Identify the blood parasite species.
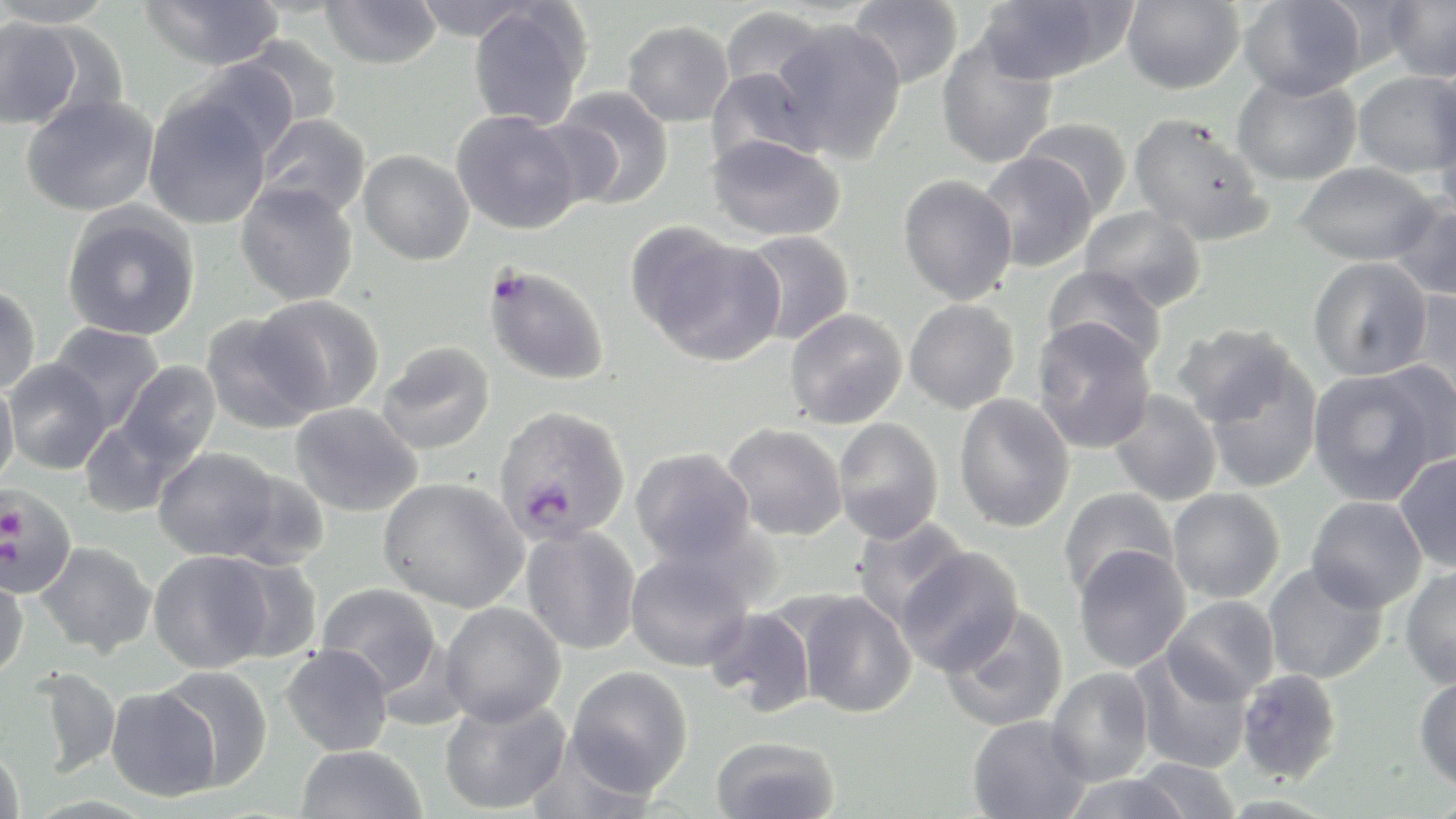

Plasmodium falciparum.

Approximate bounding boxes as named x1/y1/x2/y2 corners in pixels. Uninfected red blood cell locations: (x1=0, y1=0, x2=119, y2=28), (x1=139, y1=0, x2=285, y2=70), (x1=321, y1=0, x2=442, y2=69), (x1=409, y1=0, x2=537, y2=42), (x1=847, y1=0, x2=964, y2=91), (x1=976, y1=0, x2=1130, y2=84), (x1=1121, y1=0, x2=1244, y2=94), (x1=1316, y1=0, x2=1421, y2=74), (x1=1383, y1=0, x2=1456, y2=83), (x1=1238, y1=1, x2=1368, y2=100), (x1=467, y1=3, x2=592, y2=131), (x1=718, y1=5, x2=833, y2=104), (x1=0, y1=17, x2=83, y2=130), (x1=622, y1=20, x2=733, y2=127), (x1=770, y1=20, x2=907, y2=163), (x1=233, y1=33, x2=345, y2=131), (x1=936, y1=36, x2=1059, y2=169), (x1=181, y1=60, x2=299, y2=162), (x1=705, y1=66, x2=822, y2=169), (x1=1352, y1=71, x2=1455, y2=178), (x1=1231, y1=73, x2=1362, y2=186), (x1=551, y1=86, x2=675, y2=210), (x1=143, y1=91, x2=273, y2=230), (x1=20, y1=94, x2=159, y2=217), (x1=1431, y1=96, x2=1456, y2=222), (x1=451, y1=110, x2=583, y2=235), (x1=1129, y1=112, x2=1271, y2=245), (x1=255, y1=114, x2=371, y2=220), (x1=1019, y1=117, x2=1132, y2=219), (x1=705, y1=133, x2=846, y2=241), (x1=358, y1=149, x2=474, y2=265), (x1=977, y1=151, x2=1098, y2=272), (x1=1294, y1=161, x2=1438, y2=266), (x1=898, y1=174, x2=1018, y2=305), (x1=235, y1=181, x2=359, y2=306), (x1=1388, y1=196, x2=1456, y2=302), (x1=61, y1=204, x2=201, y2=341), (x1=1079, y1=204, x2=1207, y2=311), (x1=629, y1=225, x2=784, y2=367), (x1=740, y1=230, x2=855, y2=345), (x1=1308, y1=257, x2=1433, y2=382), (x1=1042, y1=264, x2=1168, y2=369), (x1=0, y1=284, x2=41, y2=395), (x1=1399, y1=289, x2=1456, y2=410), (x1=252, y1=294, x2=385, y2=417), (x1=904, y1=299, x2=1020, y2=413), (x1=784, y1=308, x2=909, y2=429), (x1=199, y1=310, x2=323, y2=433), (x1=1031, y1=319, x2=1157, y2=453), (x1=48, y1=323, x2=165, y2=431), (x1=1172, y1=323, x2=1301, y2=429), (x1=376, y1=341, x2=496, y2=455), (x1=1199, y1=351, x2=1323, y2=493), (x1=1369, y1=358, x2=1456, y2=471), (x1=2, y1=359, x2=111, y2=474), (x1=118, y1=361, x2=221, y2=466), (x1=1308, y1=369, x2=1444, y2=506), (x1=0, y1=378, x2=19, y2=487), (x1=1109, y1=389, x2=1223, y2=507), (x1=953, y1=393, x2=1075, y2=533), (x1=289, y1=401, x2=424, y2=517), (x1=78, y1=417, x2=187, y2=518), (x1=833, y1=417, x2=944, y2=544), (x1=721, y1=422, x2=847, y2=541), (x1=153, y1=446, x2=280, y2=561), (x1=630, y1=447, x2=756, y2=567), (x1=1394, y1=453, x2=1456, y2=573), (x1=222, y1=468, x2=331, y2=571), (x1=378, y1=477, x2=529, y2=612), (x1=1058, y1=487, x2=1178, y2=598), (x1=1167, y1=488, x2=1285, y2=603), (x1=1305, y1=495, x2=1428, y2=613), (x1=850, y1=516, x2=970, y2=630), (x1=521, y1=526, x2=641, y2=654), (x1=35, y1=541, x2=157, y2=657), (x1=1073, y1=545, x2=1191, y2=672), (x1=895, y1=546, x2=1025, y2=676), (x1=625, y1=549, x2=755, y2=672), (x1=148, y1=550, x2=274, y2=673), (x1=216, y1=555, x2=324, y2=663), (x1=1262, y1=562, x2=1388, y2=684), (x1=1400, y1=563, x2=1456, y2=689), (x1=0, y1=575, x2=29, y2=681), (x1=316, y1=582, x2=441, y2=694), (x1=794, y1=590, x2=917, y2=718), (x1=1162, y1=596, x2=1279, y2=703), (x1=440, y1=602, x2=566, y2=726), (x1=940, y1=604, x2=1069, y2=733), (x1=703, y1=606, x2=817, y2=716), (x1=281, y1=645, x2=394, y2=756), (x1=1129, y1=648, x2=1254, y2=774), (x1=565, y1=665, x2=694, y2=797), (x1=31, y1=666, x2=121, y2=778), (x1=155, y1=666, x2=274, y2=791), (x1=1046, y1=667, x2=1154, y2=786), (x1=1236, y1=669, x2=1343, y2=784), (x1=1413, y1=672, x2=1456, y2=790), (x1=105, y1=684, x2=221, y2=802), (x1=439, y1=696, x2=570, y2=815), (x1=967, y1=715, x2=1093, y2=819), (x1=710, y1=736, x2=840, y2=819), (x1=295, y1=745, x2=427, y2=819), (x1=0, y1=748, x2=25, y2=819), (x1=1129, y1=757, x2=1241, y2=819), (x1=1060, y1=772, x2=1193, y2=819). Plasmodium falciparum-infected red blood cell locations: (x1=482, y1=264, x2=610, y2=386), (x1=492, y1=405, x2=631, y2=547), (x1=0, y1=484, x2=76, y2=598). May-Grünwald-Giemsa-stained preparation. Single field of view. Image is 1456×819 pixels. Optical microscopy. Thin blood smear. 1000x magnification.